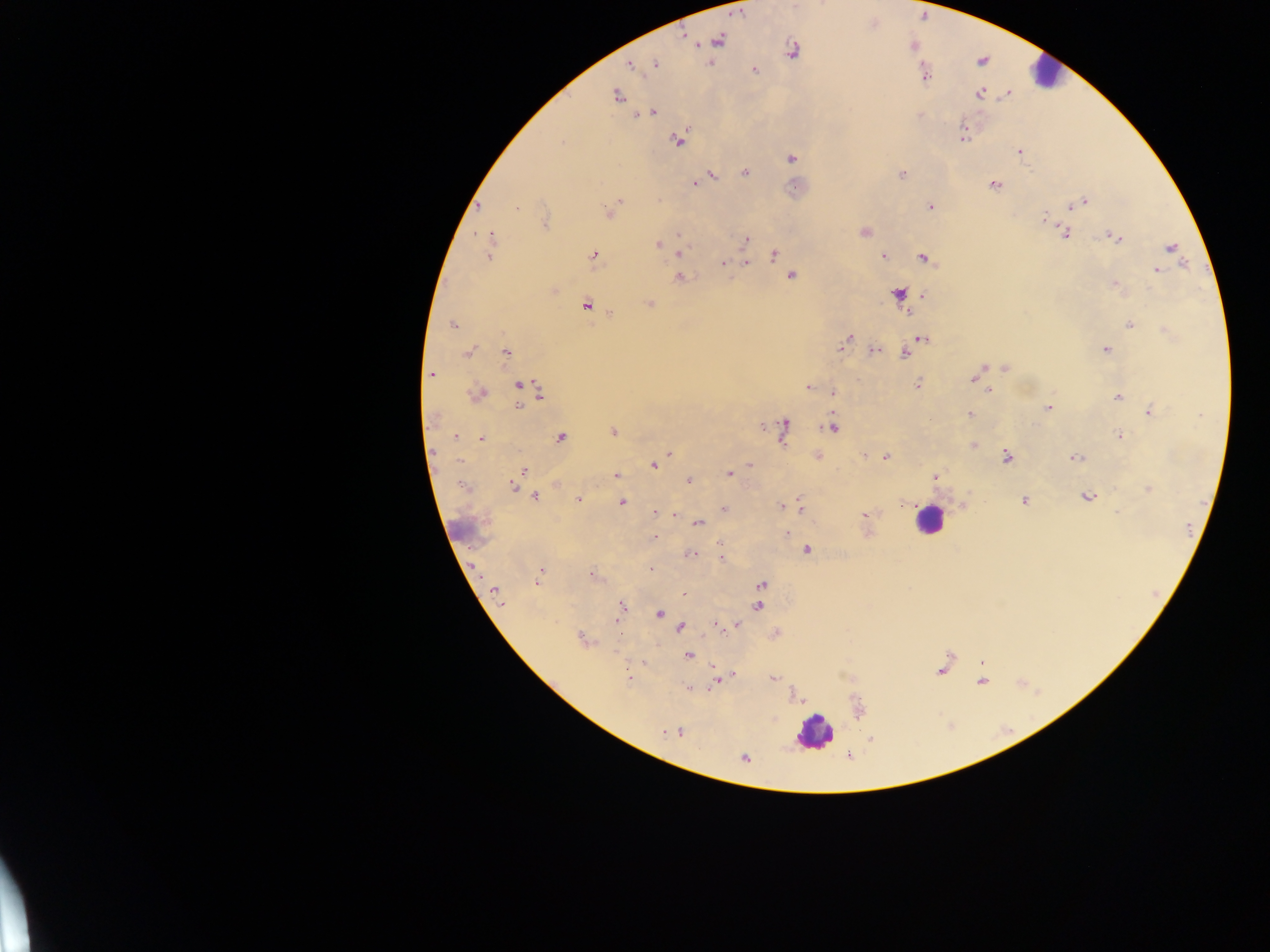

leukocyte_locations: 'approximate centers as x y in pixels: 1045 74; 929 519; 462 530; 815 732'
field_of_view: single
preparation: thick blood film
capture: mobile-phone photograph through a microscope
image_size: 1270×952 pixels
malaria_parasite_locations: 'approximate centers as x y in pixels: 719 40; 793 51; 655 64; 631 65; 754 69; 924 76; 979 94; 616 96; 651 112; 962 134; 679 140; 1018 151; 792 159; 744 172; 711 175; 901 175; 695 183; 995 185; 620 200; 1083 202; 1076 204; 478 206; 930 207; 1071 207; 516 208; 613 208; 609 213; 1044 218; 544 222; 865 232; 1064 234; 679 235; 490 237; 1116 238; 746 240; 658 244; 1171 247; 681 251; 490 253; 774 254; 594 256; 883 256; 924 258; 723 262; 747 263; 783 266; 1157 270; 791 276; 679 278; 1115 284; 898 293; 923 295; 649 303; 586 304; 904 308; 907 312; 612 313; 453 325; 1129 325; 921 339; 845 342; 873 350; 1106 350; 505 351; 468 352; 904 354; 1005 368; 431 373; 973 378; 917 384; 519 385; 809 388; 990 390; 833 392; 478 393; 541 394; 1117 397; 518 407; 1049 408; 1149 412; 970 414; 1201 415; 784 426; 831 428; 613 431; 783 433; 455 436; 1119 436; 560 438; 480 439; 973 444; 669 452; 1007 456; 886 457; 1075 458; 460 460; 653 465; 750 465; 524 470; 729 474; 616 476; 935 476; 688 481; 462 486; 512 486; 1148 489; 535 496; 1088 497; 579 499; 1024 500; 622 502; 903 504; 781 507; 724 508; 800 508; 654 514; 674 515; 865 515; 697 523; 786 533; 655 538; 807 550; 690 554; 720 557; 652 569; 541 571; 592 575; 537 582; 761 584; 494 591; 685 594; 502 602; 621 606; 759 606; 659 614; 617 620; 716 625; 735 625; 680 628; 581 639; 689 654; 734 674; 628 678; 718 678; 773 678; 689 687; 679 732; 663 733; 743 758'
country: Ghana